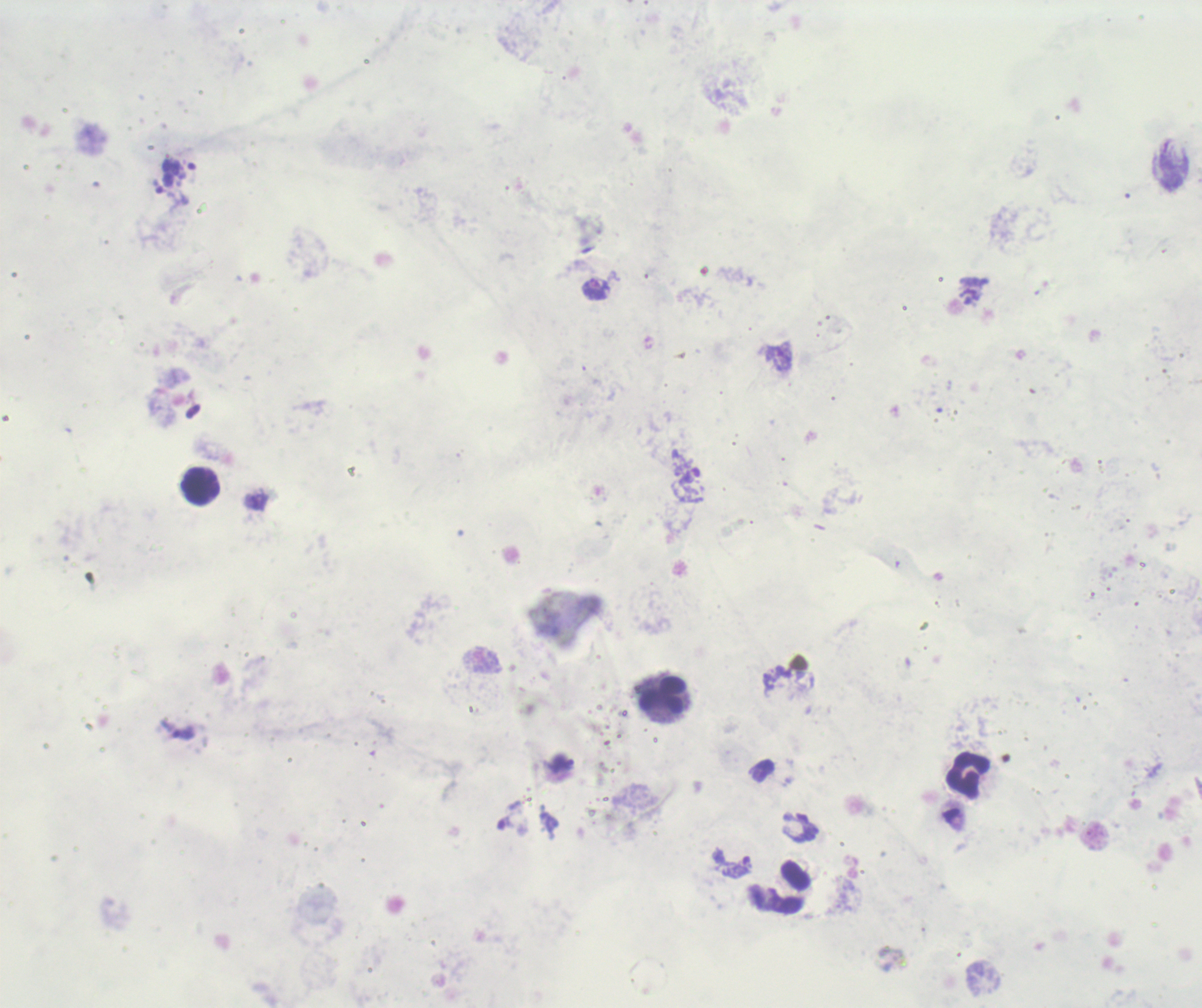

{
  "result": "malaria parasites detected",
  "background_quality": "poor",
  "preparation": "thick blood film",
  "leukocyte_locations": "approximate centers as {x, y} in pixels: {200, 486}, {662, 695}, {968, 776}, {785, 888}",
  "context": "previously used in a real diagnosis",
  "image_size": "1202×1008 pixels",
  "trophozoite_locations": "approximate centers as {x, y} in pixels: {158, 185}, {596, 289}, {183, 734}, {737, 868}",
  "stain": "Romanowsky",
  "magnification": "100x",
  "field_of_view": "single"
}